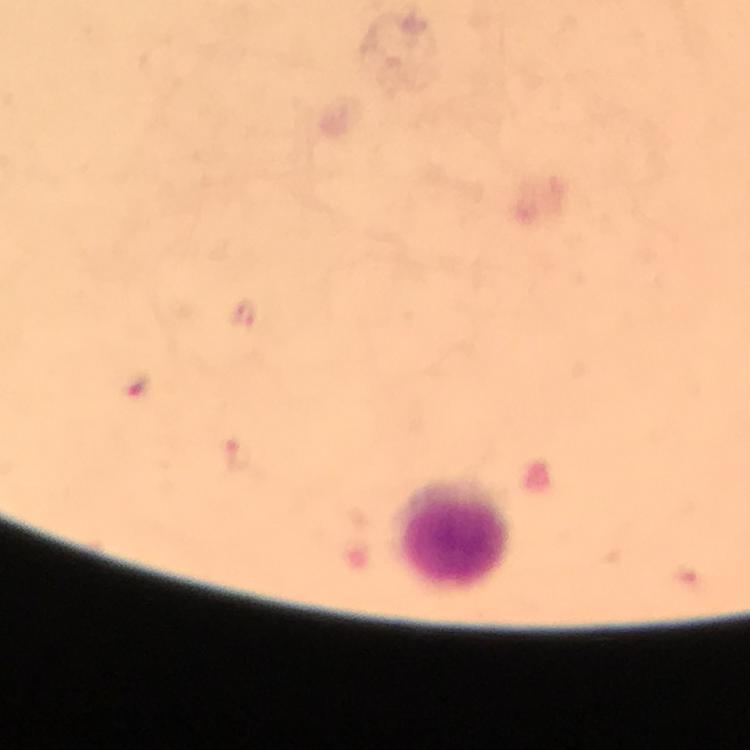

Approximate centers as (x, y) in pixels.
Summary:
  - Leukocyte locations: (448, 530)
  - Cropped from: a single field of view
  - Capture: smartphone camera through the microscope
  - Preparation: thick smear
  - Image size: 750×750 pixels
  - Malaria parasites: none detected
  - Immersion oil: used
  - Magnification: 100x
  - Context: from a diagnostic examination for malaria
  - Stain: Giemsa